Classify this cell by malaria status.
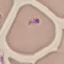

Uninfected.

image_type: automatically extracted cell patch, resized to 64 × 64 pixels
preparation: thin smear
stain: Giemsa
capture: smartphone camera at the microscope eyepiece